Report the malaria status of this cell.
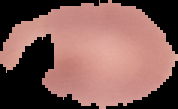

Uninfected.

preparation = thin blood smear
image size = 178×109 pixels
image type = cell region segmented out of the field of view; surrounding area masked to black